Assess this cell for malaria.
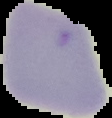
It is uninfected.

The area outside the segmented cell region is set to black. Image is 112×118 pixels. From a thin blood smear.